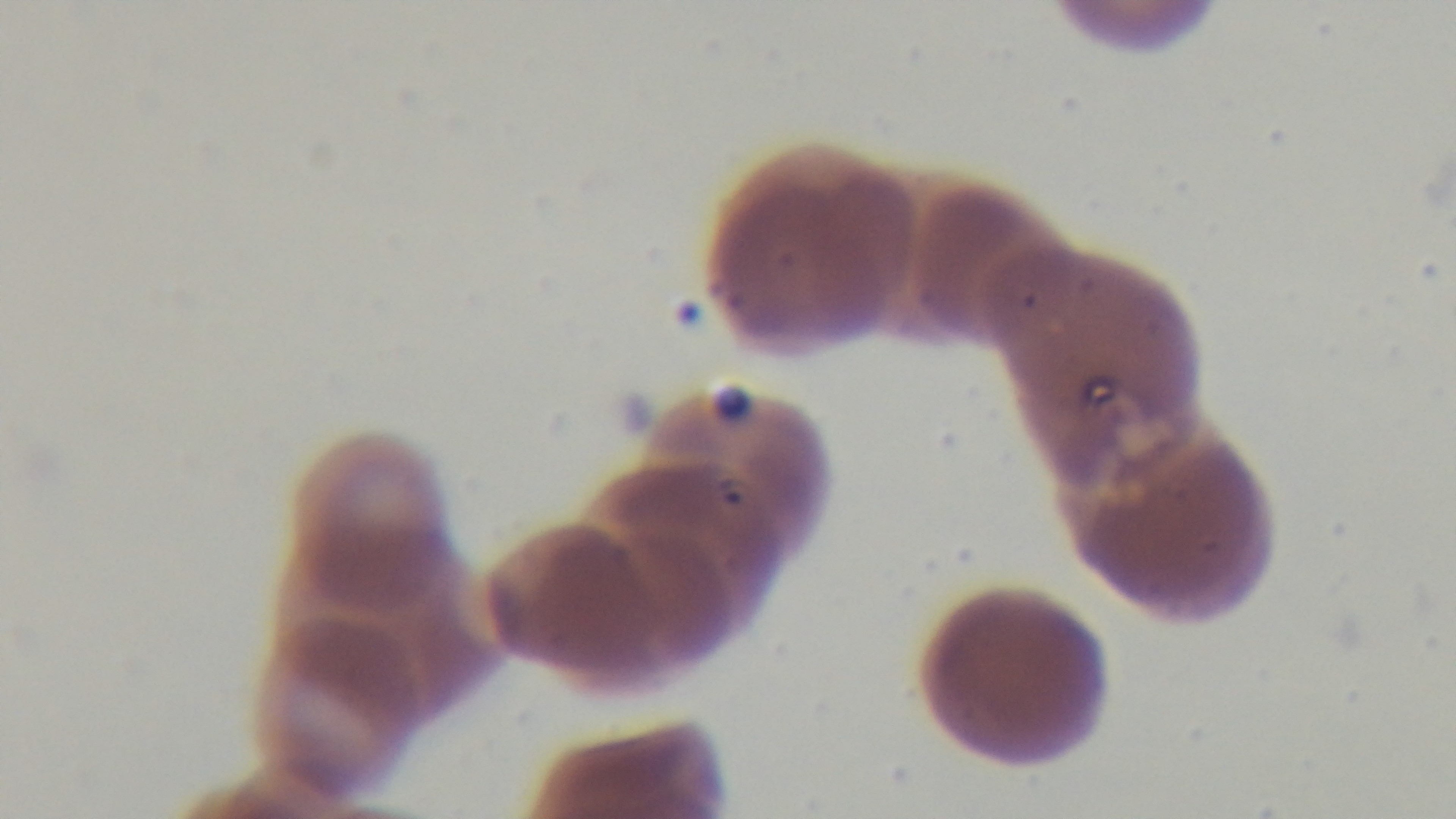

Light microscopy. Single field of view. Captured with a mounted 4K digital camera. Preparation: thin smear. Malaria status: positive. Oil-immersion objective, 100x. Giemsa-stained.